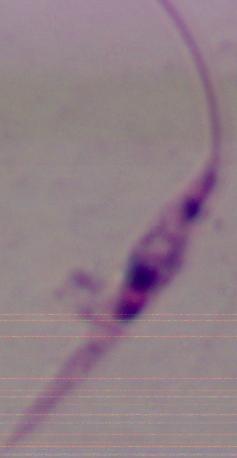 A Leishmania parasite is seen. 1000x magnification. Micrograph.